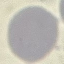
result: no malaria parasites detected
stain: Giemsa
capture: smartphone through the microscope eyepiece
preparation: thin blood smear
image_type: cell patch, automatically extracted from a larger field of view and resized to 64 × 64 pixels